Report the malaria status of this cell.
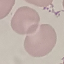
Uninfected.

Thin blood film. Automatically extracted cell patch, resized to 64 × 64 pixels. Giemsa stain. Acquired by smartphone through the microscope eyepiece.